Name the parasite shown.
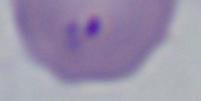

This is Babesia.

1000x magnification. Micrograph.